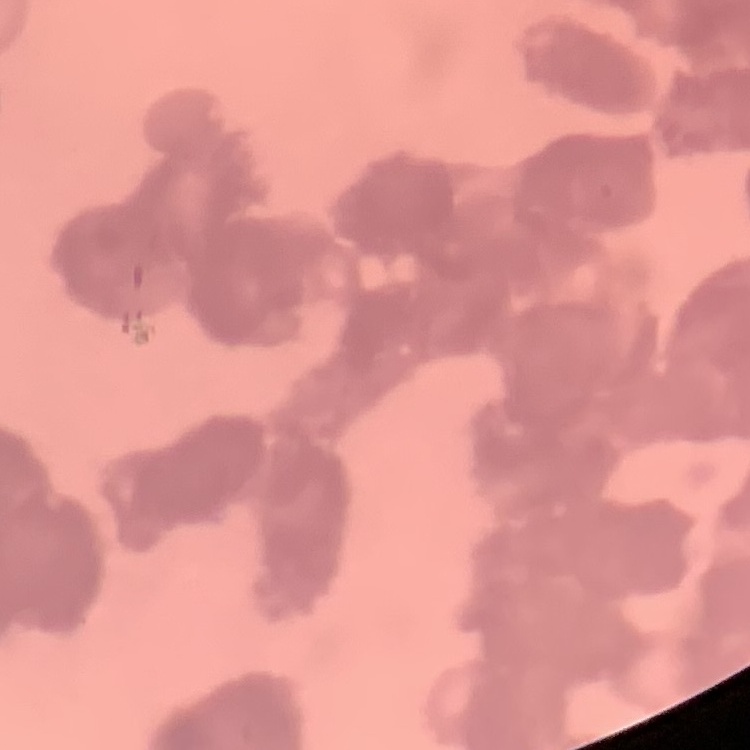

{
  "erythrocyte_morphology": "rouleaux formation",
  "preparation": "thin blood smear",
  "image_type": "square crop of a larger photomicrograph",
  "stain": "Field's or Giemsa"
}